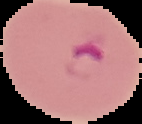
{
  "image_type": "segmented cell region on a black background",
  "malaria_status": "parasitized",
  "image_size": "142×124 pixels",
  "preparation": "thin blood smear"
}